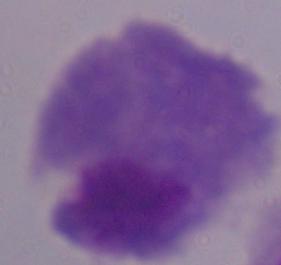

identification = trichomonad
modality = photomicrograph
magnification = 1000x